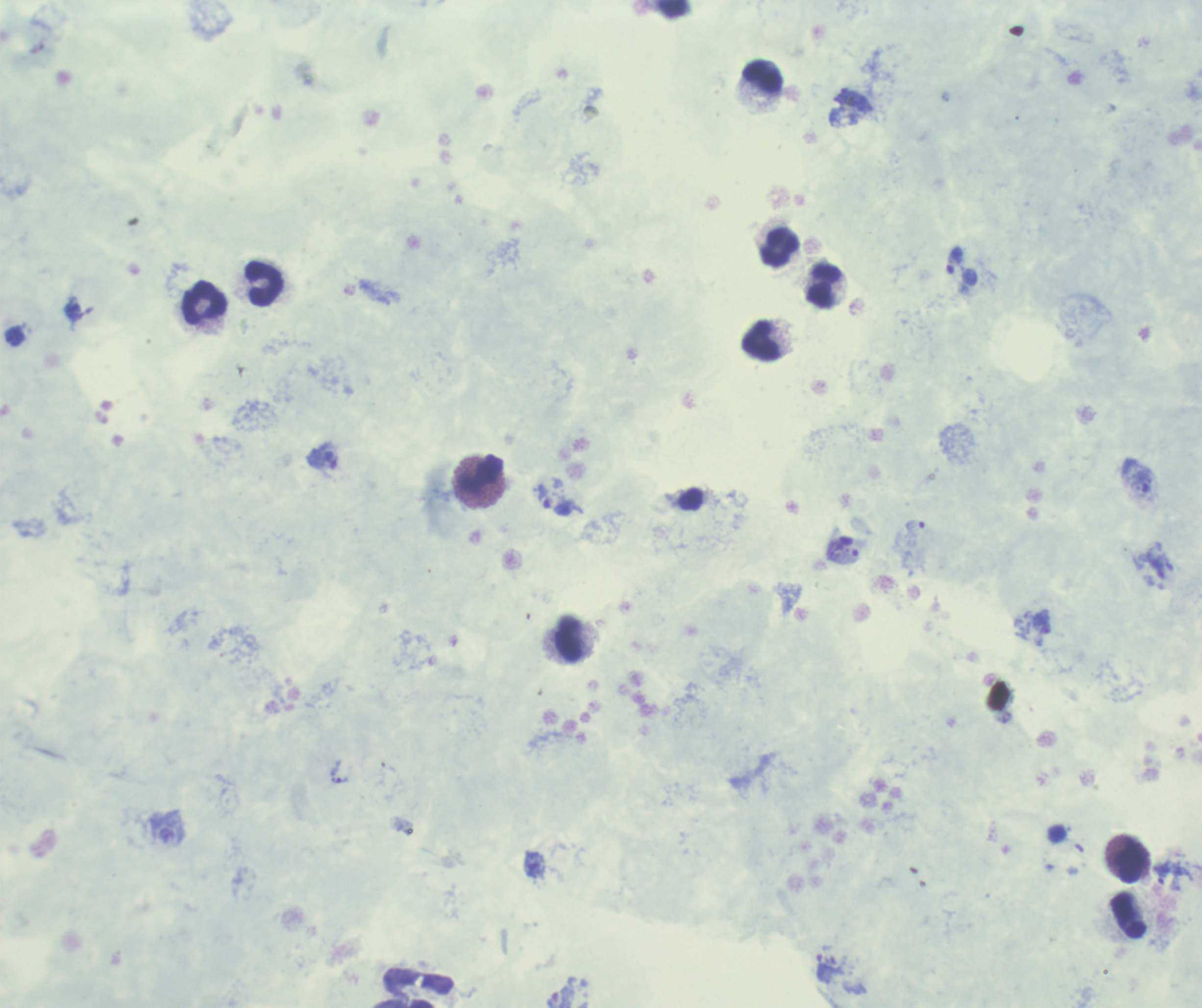

result: positive for Plasmodium parasites
field_of_view: single
trophozoite_locations: 'approximate centers as (x, y) in pixels: (955, 261), (14, 338), (323, 464), (1139, 481), (561, 508), (342, 780), (536, 866), (1161, 873), (836, 966)'
leukocyte_locations: 'approximate centers as (x, y) in pixels: (763, 77), (781, 248), (264, 283), (824, 287), (205, 303), (762, 341), (480, 474), (569, 641), (1131, 862), (1129, 917), (413, 988)'
magnification: 100x
background_quality: unsatisfactory
context: previously used in a real diagnosis
image_size: 1202×1008 pixels
stain: Romanowsky
preparation: thick blood smear